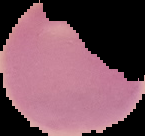

image_type: segmented cell region with the area outside set to black
malaria_status: uninfected
image_size: 145×136 pixels
preparation: thin blood film